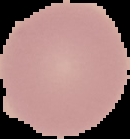

image_size: 130×139 pixels
image_type: segmented cell region with the area outside set to black
result: negative for Plasmodium parasites
preparation: thin blood smear